Classify this cell by malaria status.
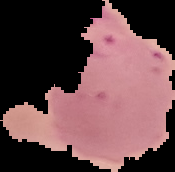

It is parasitized.

From a thin blood smear. The area outside the segmented cell region is set to black. Image is 175×172 pixels.